Locate every Plasmodium falciparum parasite and identify its life-cycle stage.
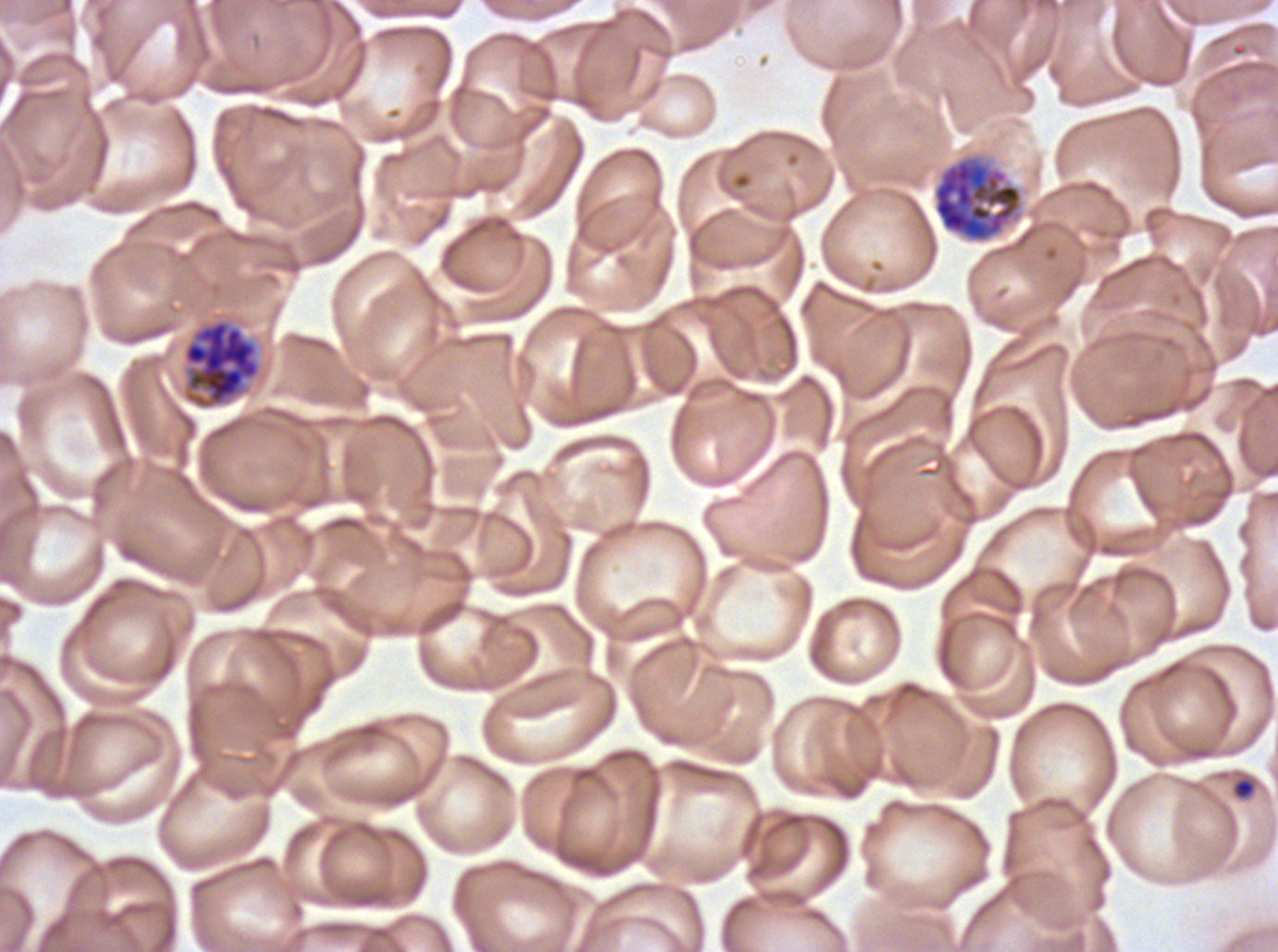
Approximate bounding boxes as {x1, y1, x2, y2} in pixels.
Rings: {1231, 776, 1257, 800}.
Late schizonts: {932, 156, 1023, 243}, {182, 318, 261, 409}.
No late-ring/early-trophozoite forms, mid trophozoites, late trophozoites, early schizonts, segmenters, or gametocytes observed.

Plasmodium falciparum from a patient in The Gambia, cultured ex vivo for 24 to 48 hours. Thin blood film. Life-cycle stages observed: ring, late schizont. Image is 1278×952 pixels. One sub-image of a larger composite. Giemsa stain.